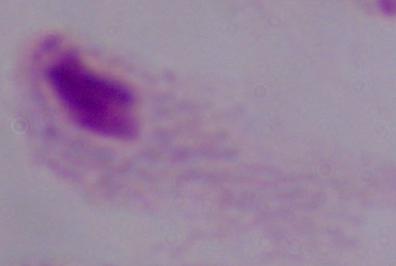

Photomicrograph. Captured at 1000x magnification. A trichomonad is shown.